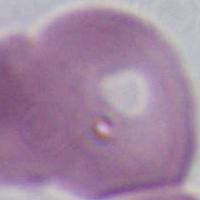

{
  "magnification": "1000x",
  "identification": "erythrocyte",
  "modality": "photomicrograph"
}